Assess this cell for malaria.
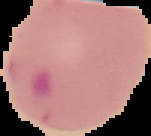

Parasitized.

From a thin blood film. Image is 151×136 pixels. The area outside the segmented cell region is set to black.